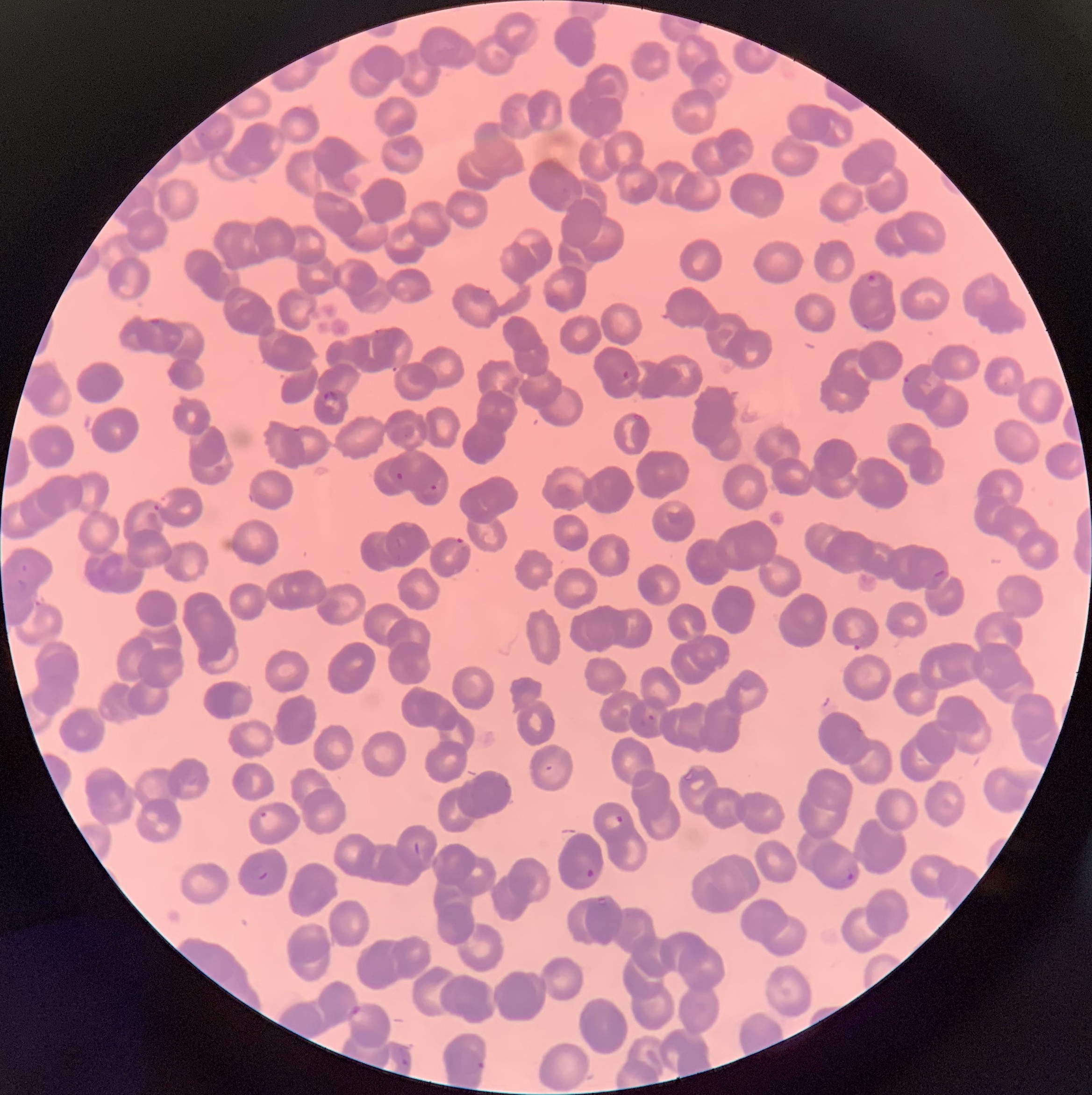

Approximate bounding boxes as (x1, y1, x2, y2) in pixels. Plasmodium parasite locations: (866, 274, 885, 289), (860, 322, 874, 330), (371, 329, 387, 337), (621, 369, 631, 381), (902, 374, 912, 386), (322, 389, 342, 407), (395, 472, 404, 480), (423, 485, 438, 499), (152, 504, 160, 512), (454, 537, 467, 549), (16, 560, 31, 592), (931, 569, 946, 581), (640, 714, 656, 726), (258, 810, 268, 819), (602, 813, 624, 832), (253, 865, 271, 882), (584, 868, 595, 878), (838, 871, 855, 884), (349, 1005, 373, 1024), (401, 1059, 409, 1067), (476, 1061, 485, 1070). Optical microscopy. The red blood cells show rouleaux formation. Thin blood smear. Image is 1092×1095 pixels.